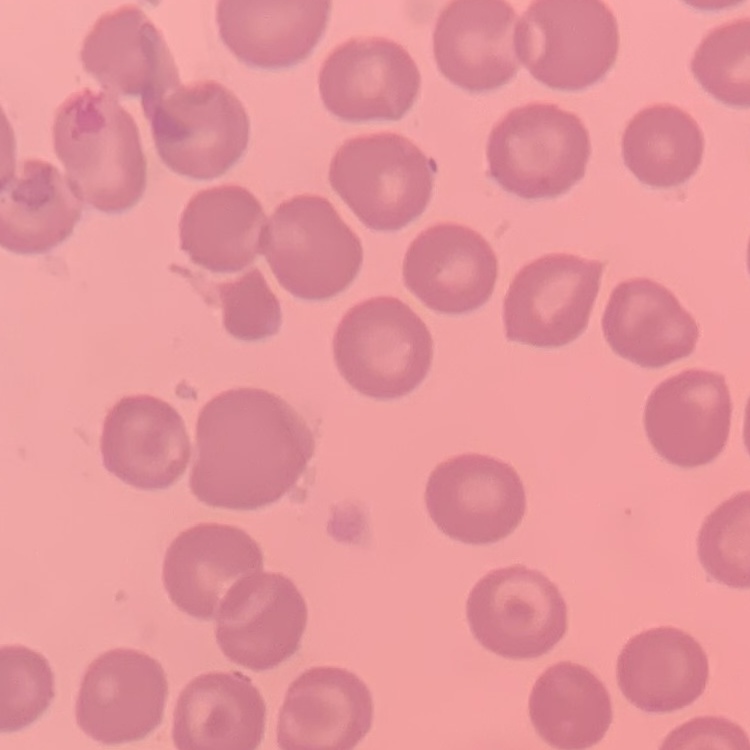

erythrocyte morphology = no rouleaux formation
image type = square crop of a larger photomicrograph
preparation = thin blood smear
stain = Field's or Giemsa